Name the parasite shown.
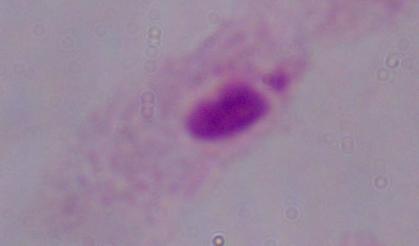
This is a trichomonad.

Summary:
  - Modality: micrograph
  - Magnification: 1000x